Locate every leukocyte (white blood cell).
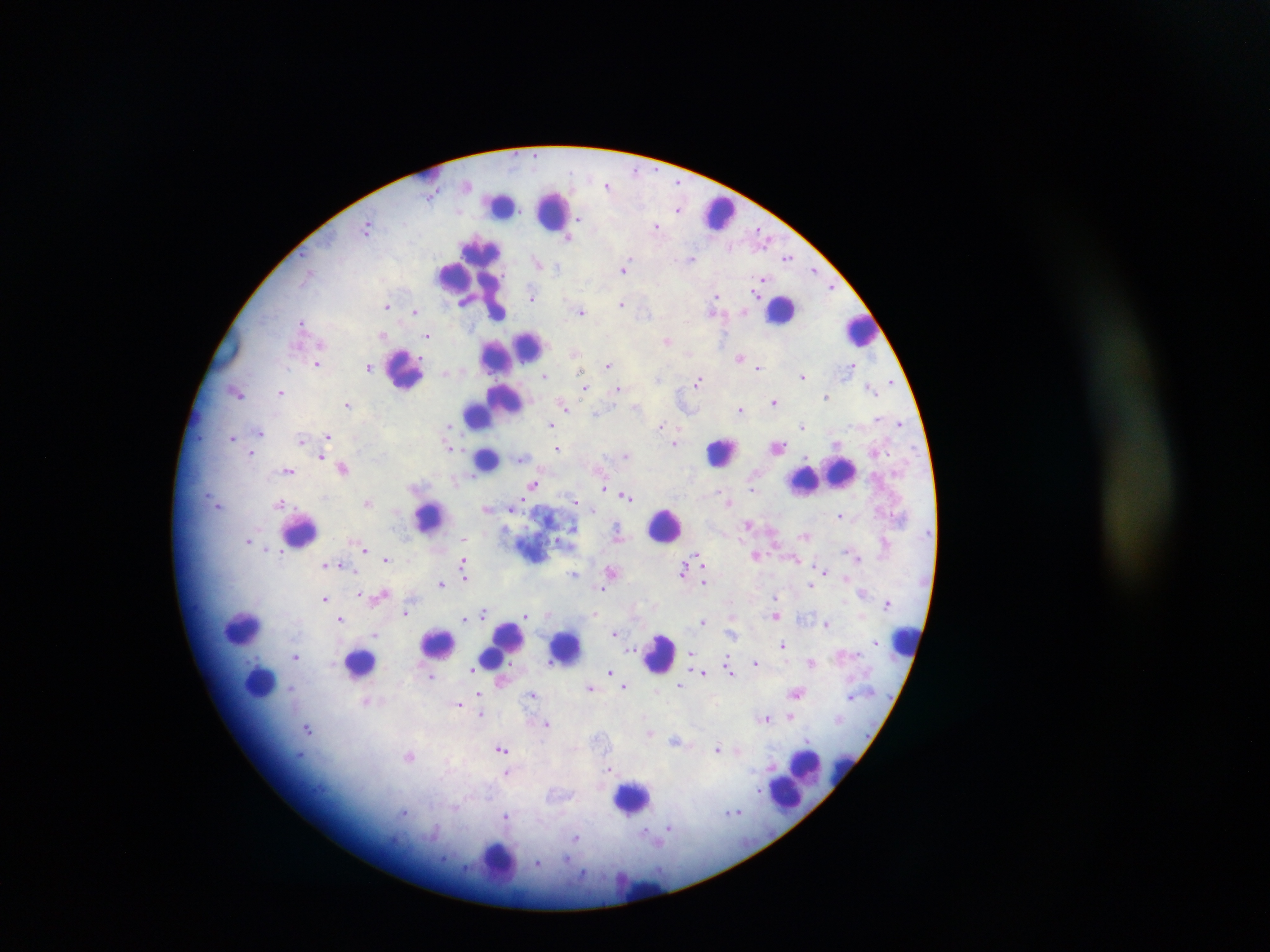
Approximate centers as {x, y} in pixels.
Leukocytes: {426, 172}, {501, 204}, {552, 209}, {717, 213}, {482, 249}, {454, 275}, {468, 276}, {489, 293}, {497, 309}, {782, 310}, {860, 330}, {528, 345}, {497, 357}, {404, 370}, {504, 397}, {493, 405}, {478, 414}, {722, 451}, {487, 459}, {837, 473}, {812, 476}, {804, 479}, {430, 516}, {665, 525}, {299, 530}, {243, 627}, {906, 641}, {438, 643}, {502, 645}, {565, 646}, {660, 654}, {360, 661}, {259, 682}, {806, 770}, {794, 781}, {786, 792}, {631, 798}, {498, 860}, {639, 887}.

Summary:
  - Malaria parasite locations: {636, 171}, {608, 184}, {678, 208}, {368, 226}, {656, 226}, {762, 233}, {569, 237}, {692, 257}, {787, 257}, {539, 263}, {625, 268}, {814, 270}, {764, 277}, {832, 287}, {756, 289}, {756, 294}, {717, 296}, {531, 297}, {387, 304}, {623, 304}, {581, 311}, {417, 312}, {714, 312}, {302, 322}, {385, 336}, {427, 336}, {667, 340}, {575, 351}, {740, 358}, {318, 363}, {608, 365}, {854, 365}, {370, 366}, {759, 368}, {446, 373}, {543, 375}, {804, 376}, {697, 381}, {891, 381}, {584, 386}, {871, 387}, {618, 389}, {236, 391}, {281, 392}, {827, 396}, {774, 401}, {348, 404}, {564, 406}, {740, 409}, {596, 414}, {449, 424}, {899, 424}, {550, 425}, {661, 425}, {802, 426}, {261, 431}, {328, 436}, {233, 438}, {302, 439}, {675, 443}, {837, 443}, {450, 445}, {777, 447}, {558, 448}, {252, 453}, {626, 455}, {322, 457}, {521, 458}, {343, 467}, {289, 470}, {533, 484}, {752, 487}, {606, 488}, {626, 496}, {369, 502}, {576, 502}, {729, 502}, {217, 503}, {281, 503}, {515, 508}, {488, 509}, {840, 516}, {749, 524}, {573, 527}, {618, 533}, {804, 535}, {559, 540}, {249, 541}, {885, 541}, {267, 549}, {365, 550}, {280, 551}, {697, 555}, {757, 555}, {858, 557}, {386, 558}, {795, 558}, {464, 562}, {701, 564}, {326, 565}, {683, 568}, {611, 570}, {823, 571}, {465, 572}, {573, 573}, {845, 576}, {704, 582}, {441, 583}, {812, 585}, {602, 588}, {863, 592}, {361, 594}, {381, 594}, {774, 597}, {325, 599}, {887, 602}, {406, 612}, {594, 613}, {483, 614}, {861, 614}, {528, 615}, {775, 615}, {339, 618}, {464, 619}, {703, 621}, {827, 623}, {615, 632}, {732, 634}, {376, 635}, {877, 642}, {783, 645}, {629, 648}, {691, 653}, {296, 655}, {728, 660}, {812, 661}, {756, 662}, {513, 664}, {471, 671}, {610, 671}, {702, 672}, {731, 673}, {431, 676}, {682, 685}, {590, 686}, {624, 686}, {290, 687}, {797, 691}, {481, 693}, {533, 695}, {851, 696}, {366, 701}, {458, 704}, {481, 713}, {790, 716}, {766, 718}, {546, 724}, {308, 727}, {650, 733}, {804, 740}, {677, 741}, {719, 748}, {503, 750}, {738, 751}, {410, 757}, {610, 767}, {773, 767}, {506, 774}, {757, 790}, {405, 812}, {734, 812}, {506, 815}, {669, 828}, {577, 838}, {538, 862}
  - Preparation: thick blood smear
  - Image size: 1270×952 pixels
  - Country: Ghana
  - Field of view: single
  - Capture: mobile-phone photograph through a microscope